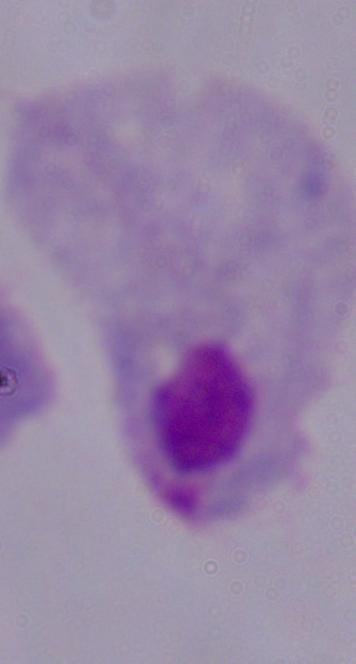

1000x magnification. Micrograph. A trichomonad is shown.